Classify this cell by malaria status.
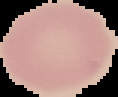
It is uninfected.

Summary:
  - Image size: 118×97 pixels
  - Preparation: thin blood film
  - Image type: segmented cell region on a black background